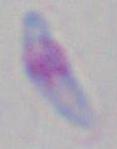

Summary:
  - Magnification: 1000x
  - Modality: photomicrograph
  - Identification: Toxoplasma gondii